Evaluate for malaria.
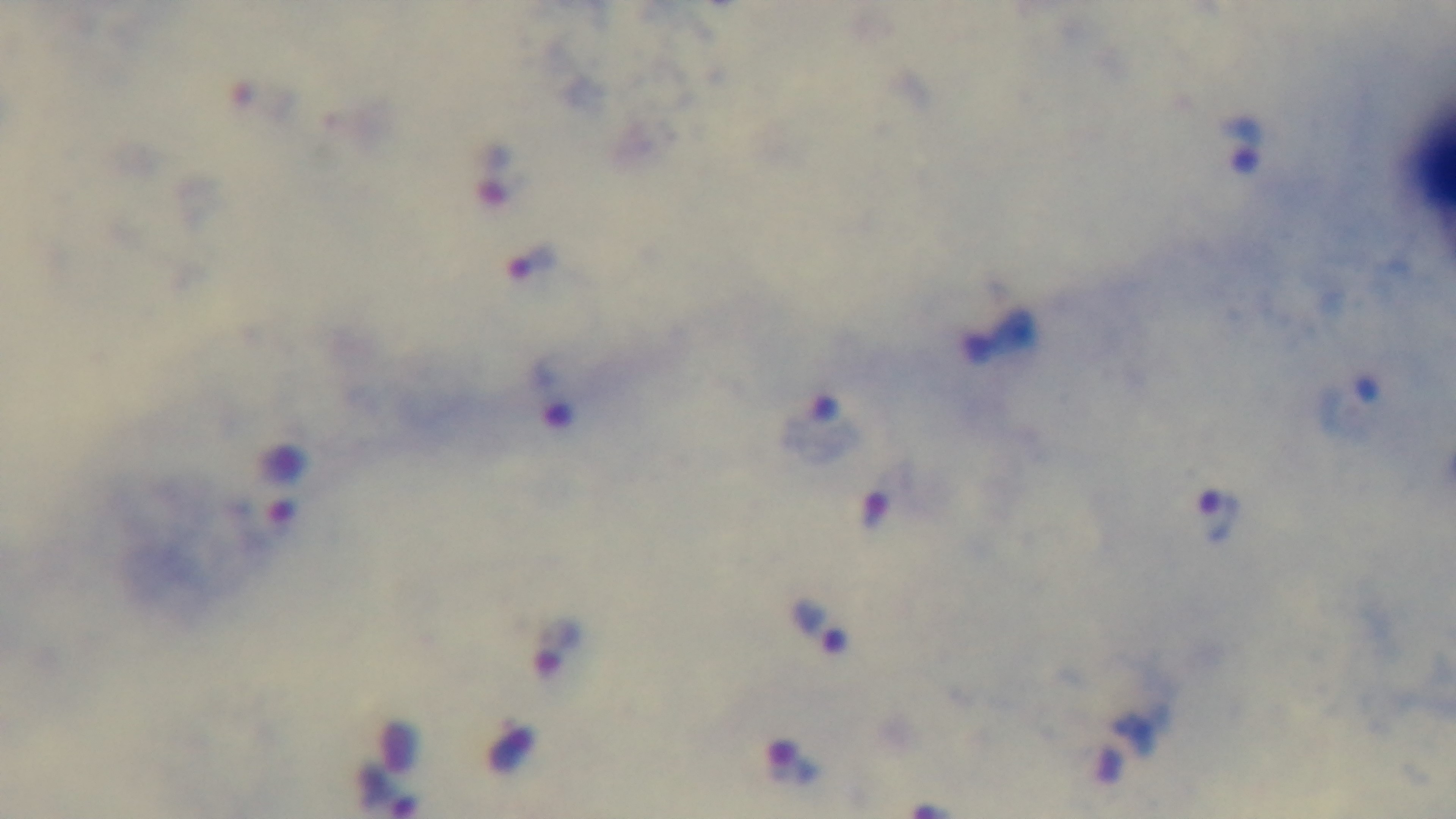

It is infected.

Summary:
  - Stain: Giemsa
  - Preparation: thick blood film
  - Capture: mounted 4K digital camera
  - Objective: 100x oil immersion
  - Field of view: single
  - Modality: light microscopy